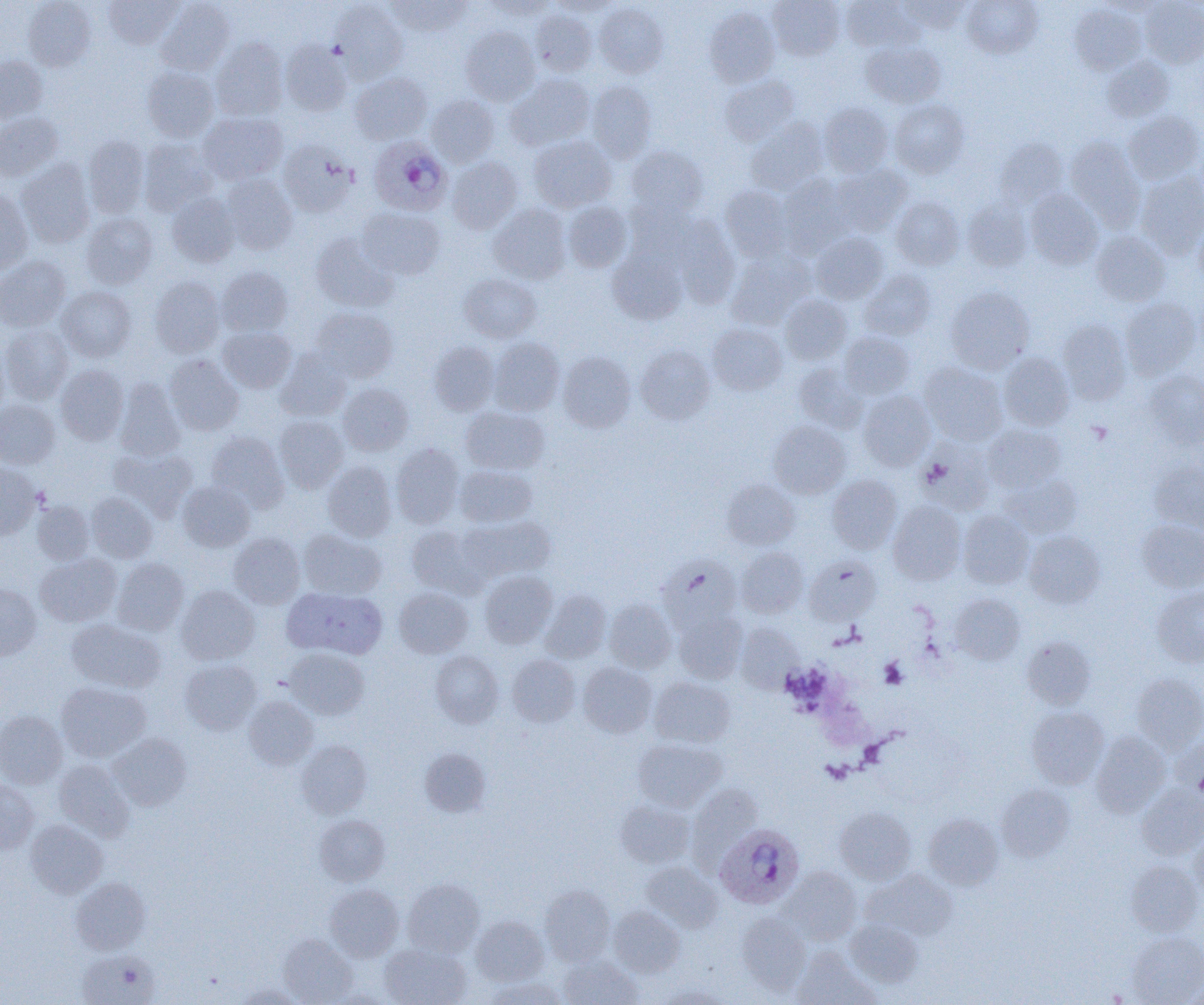
slide-level diagnosis = Plasmodium ovale
platelet locations = approximate bounding boxes as (x1,y1)-(x2,y2) corner pairs in pixels: (879,658)-(907,689)
magnification = 1000x
image size = 1204×1005 pixels
field of view = one of a larger specimen
modality = light microscopy
uninfected red blood cell locations = approximate bounding boxes as (x1,y1)-(x2,y2) corner pairs in pixels: (24,0)-(96,70), (104,0)-(181,49), (387,0)-(472,36), (481,0)-(556,19), (768,0)-(844,60), (841,0)-(919,51), (899,0)-(971,33), (962,0)-(1042,58), (1140,0)-(1204,67), (156,1)-(235,75), (331,1)-(407,83), (549,1)-(620,17), (1099,1)-(1168,17), (594,2)-(669,78), (1070,3)-(1145,74), (704,7)-(780,88), (530,9)-(597,76), (460,27)-(540,105), (211,37)-(288,121), (280,39)-(352,116), (862,41)-(946,107), (1102,55)-(1174,121), (0,56)-(48,122), (142,66)-(219,142), (350,72)-(432,143), (506,74)-(594,150), (719,76)-(800,146), (587,80)-(657,162), (426,94)-(499,167), (890,99)-(969,178), (820,103)-(893,177), (1123,111)-(1204,185), (0,112)-(63,181), (198,112)-(288,185), (745,119)-(829,194), (529,135)-(616,212), (83,136)-(149,218), (1065,137)-(1145,227), (139,138)-(218,215), (995,138)-(1068,209), (278,140)-(358,217), (625,144)-(707,220), (447,157)-(522,233), (17,159)-(94,248), (831,164)-(912,235), (1136,173)-(1204,259), (221,174)-(297,255), (778,175)-(855,255), (720,185)-(793,262), (0,189)-(34,273), (1025,189)-(1103,269), (167,193)-(240,267), (891,197)-(964,270), (963,199)-(1033,271), (563,201)-(633,272), (489,204)-(572,284), (357,207)-(445,280), (82,212)-(157,289), (671,214)-(741,308), (1193,216)-(1204,286), (1091,231)-(1170,306), (811,232)-(888,303), (310,233)-(396,312), (607,249)-(687,324), (727,251)-(815,330), (0,255)-(70,331), (216,267)-(293,336), (859,270)-(936,341), (459,273)-(540,342), (150,276)-(226,358), (57,286)-(136,361), (945,286)-(1035,373), (780,294)-(852,365), (1120,298)-(1201,379), (310,307)-(398,382), (1057,319)-(1131,404), (707,323)-(787,395), (1,325)-(74,404), (217,327)-(296,393), (839,331)-(914,399), (488,337)-(564,415), (0,339)-(8,419), (429,341)-(498,414), (635,345)-(715,424), (275,350)-(352,421), (558,351)-(636,433), (999,352)-(1074,430), (164,355)-(244,436), (920,361)-(1008,445), (793,363)-(868,433), (55,365)-(128,445), (1144,370)-(1204,448), (115,378)-(186,461), (337,382)-(414,456), (858,390)-(936,471), (0,399)-(59,468), (461,406)-(549,475), (274,415)-(349,492), (769,421)-(850,499), (983,424)-(1065,492), (207,431)-(289,511), (917,436)-(996,515), (391,444)-(463,528), (111,448)-(197,520), (1149,460)-(1204,533), (323,461)-(397,541), (0,463)-(40,539), (455,464)-(538,527), (827,474)-(902,553), (1000,474)-(1082,538), (722,478)-(800,550), (177,481)-(255,552), (86,492)-(157,562), (32,500)-(94,565), (888,500)-(966,585), (958,511)-(1033,589), (459,516)-(555,583), (1137,519)-(1204,592), (407,525)-(487,596), (298,529)-(386,599), (1024,531)-(1105,608), (229,533)-(305,608), (737,547)-(808,618), (35,553)-(121,626), (658,556)-(742,630), (804,556)-(881,625), (113,558)-(189,636), (480,570)-(557,648), (0,584)-(41,660), (176,585)-(259,664), (284,586)-(388,659), (394,587)-(473,658), (1152,587)-(1204,667), (540,589)-(611,662), (950,593)-(1025,665), (605,599)-(676,672), (674,611)-(746,683), (66,619)-(165,693), (734,623)-(803,693), (1022,637)-(1095,709), (286,648)-(368,719), (430,651)-(503,727), (507,654)-(580,726), (180,660)-(261,735), (578,662)-(657,738), (1131,673)-(1204,753), (649,677)-(735,748), (56,682)-(150,762), (244,696)-(318,769), (1026,706)-(1109,788), (0,710)-(67,789), (1090,731)-(1170,816), (108,733)-(191,810), (1169,735)-(1204,797), (633,738)-(726,811), (296,741)-(372,818), (419,748)-(491,817), (55,759)-(135,841), (0,781)-(39,854), (687,783)-(762,866), (996,784)-(1075,862), (1137,784)-(1204,860), (615,799)-(695,868), (835,807)-(916,884), (924,813)-(1004,890), (314,814)-(390,886), (26,819)-(107,898), (1189,831)-(1204,900), (1126,860)-(1202,936), (640,861)-(722,932), (781,866)-(861,943), (865,869)-(958,941), (71,878)-(150,954), (403,879)-(484,957), (325,884)-(404,961), (540,885)-(615,965), (608,906)-(685,977), (737,912)-(811,994), (471,916)-(548,986), (845,918)-(924,987), (1127,931)-(1204,1004), (278,934)-(357,1004), (380,942)-(472,1005), (792,949)-(877,1005), (77,950)-(159,1005), (559,956)-(642,1004), (485,977)-(567,1005), (233,984)-(302,1005), (657,984)-(730,1004)
preparation = thin blood smear
Plasmodium ovale-infected red blood cell locations = approximate bounding boxes as (x1,y1)-(x2,y2) corner pairs in pixels: (368,136)-(452,216), (715,824)-(805,909)